Report the malaria status of this cell.
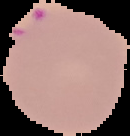

Parasitized.

From a thin blood film. Image is 130×136 pixels. The area outside the segmented cell region is set to black.